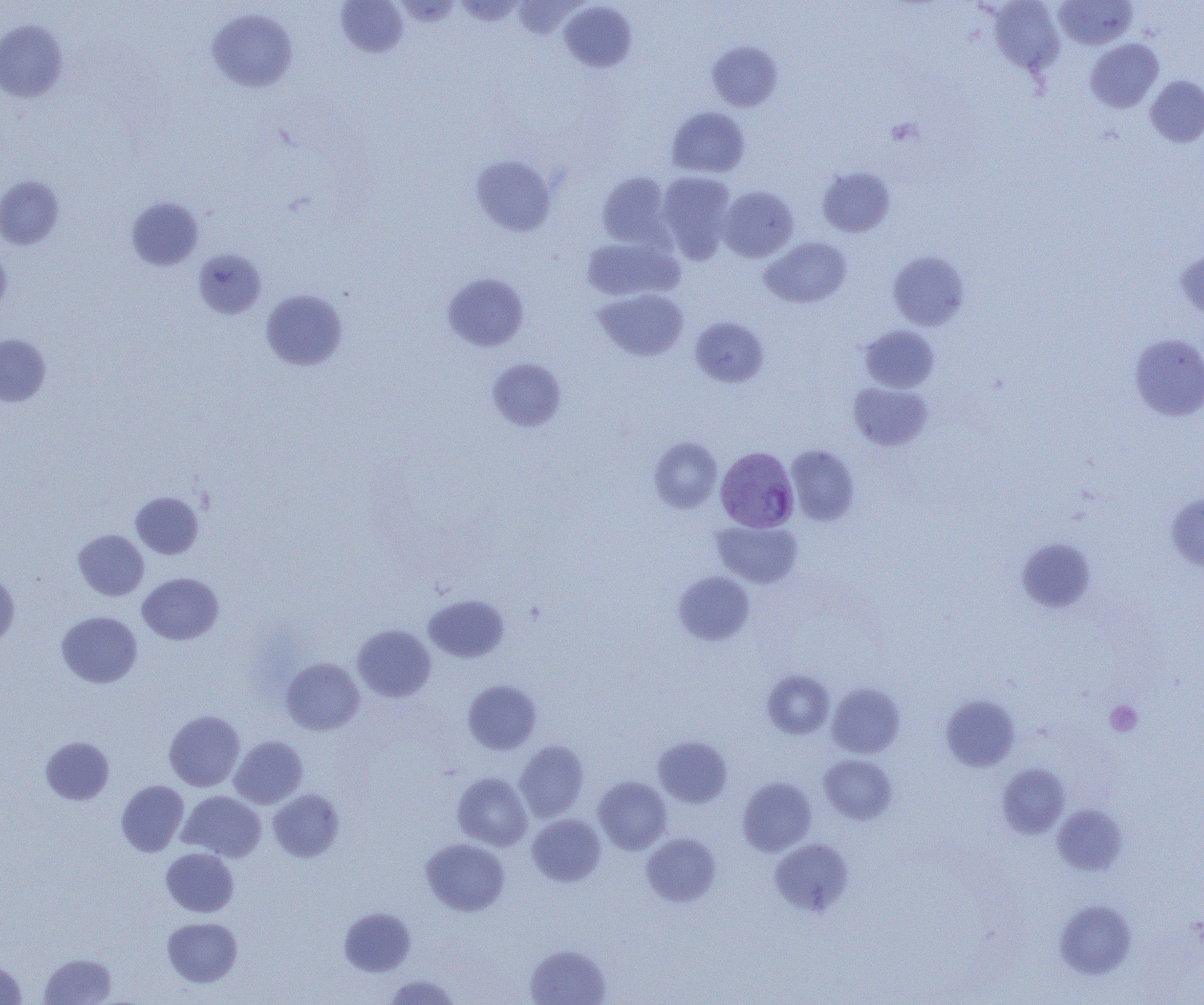

slide-level diagnosis = Plasmodium vivax
modality = light microscopy
preparation = thin blood smear
platelet locations = approximate bounding boxes as [x1, y1, x2, y2] in pixels: [1106, 701, 1142, 736]
magnification = 1000x
image size = 1204×1005 pixels
field of view = one of a larger specimen
Plasmodium vivax-infected red blood cell locations = approximate bounding boxes as [x1, y1, x2, y2] in pixels: [715, 446, 799, 532]
uninfected red blood cell locations = approximate bounding boxes as [x1, y1, x2, y2] in pixels: [336, 0, 408, 57], [455, 0, 525, 25], [988, 0, 1065, 76], [559, 1, 637, 72], [1053, 1, 1137, 49], [206, 8, 298, 92], [0, 20, 68, 102], [1085, 39, 1164, 113], [707, 42, 783, 112], [1146, 76, 1204, 147], [666, 107, 750, 177], [471, 155, 556, 236], [817, 166, 895, 237], [597, 171, 672, 248], [657, 172, 736, 262], [0, 175, 64, 249], [717, 186, 799, 262], [126, 197, 203, 271], [580, 236, 683, 302], [760, 236, 851, 308], [0, 248, 11, 319], [193, 248, 266, 319], [1175, 249, 1204, 322], [888, 250, 969, 330], [442, 272, 529, 351], [594, 288, 689, 361], [260, 289, 348, 371], [690, 317, 769, 387], [860, 325, 938, 392], [0, 334, 51, 406], [1129, 334, 1204, 420], [487, 358, 567, 431], [849, 382, 933, 451], [649, 437, 722, 513], [786, 445, 859, 525], [130, 492, 203, 559], [1166, 493, 1204, 572], [712, 520, 802, 588], [73, 529, 149, 600], [1017, 537, 1096, 614], [674, 572, 754, 644], [0, 573, 20, 649], [137, 573, 223, 644], [424, 594, 509, 662], [56, 611, 142, 688], [352, 625, 436, 702], [282, 658, 364, 735], [762, 670, 834, 739], [463, 680, 542, 754], [828, 682, 905, 758], [941, 695, 1020, 771], [164, 710, 245, 791], [653, 735, 732, 808], [229, 736, 307, 808], [41, 737, 114, 805], [514, 741, 589, 821], [819, 755, 897, 824], [997, 764, 1070, 838], [452, 772, 532, 850], [593, 777, 671, 854], [738, 777, 817, 856], [116, 780, 189, 856], [268, 789, 344, 861], [177, 791, 266, 861], [1053, 804, 1127, 875], [527, 814, 606, 886], [641, 832, 721, 906], [769, 838, 854, 916], [421, 839, 509, 916], [161, 848, 239, 917], [1055, 900, 1137, 978], [339, 906, 416, 977], [162, 918, 243, 987], [525, 944, 611, 1005], [38, 952, 117, 1005], [0, 960, 27, 1004], [382, 974, 461, 1005]